State the preparation type.
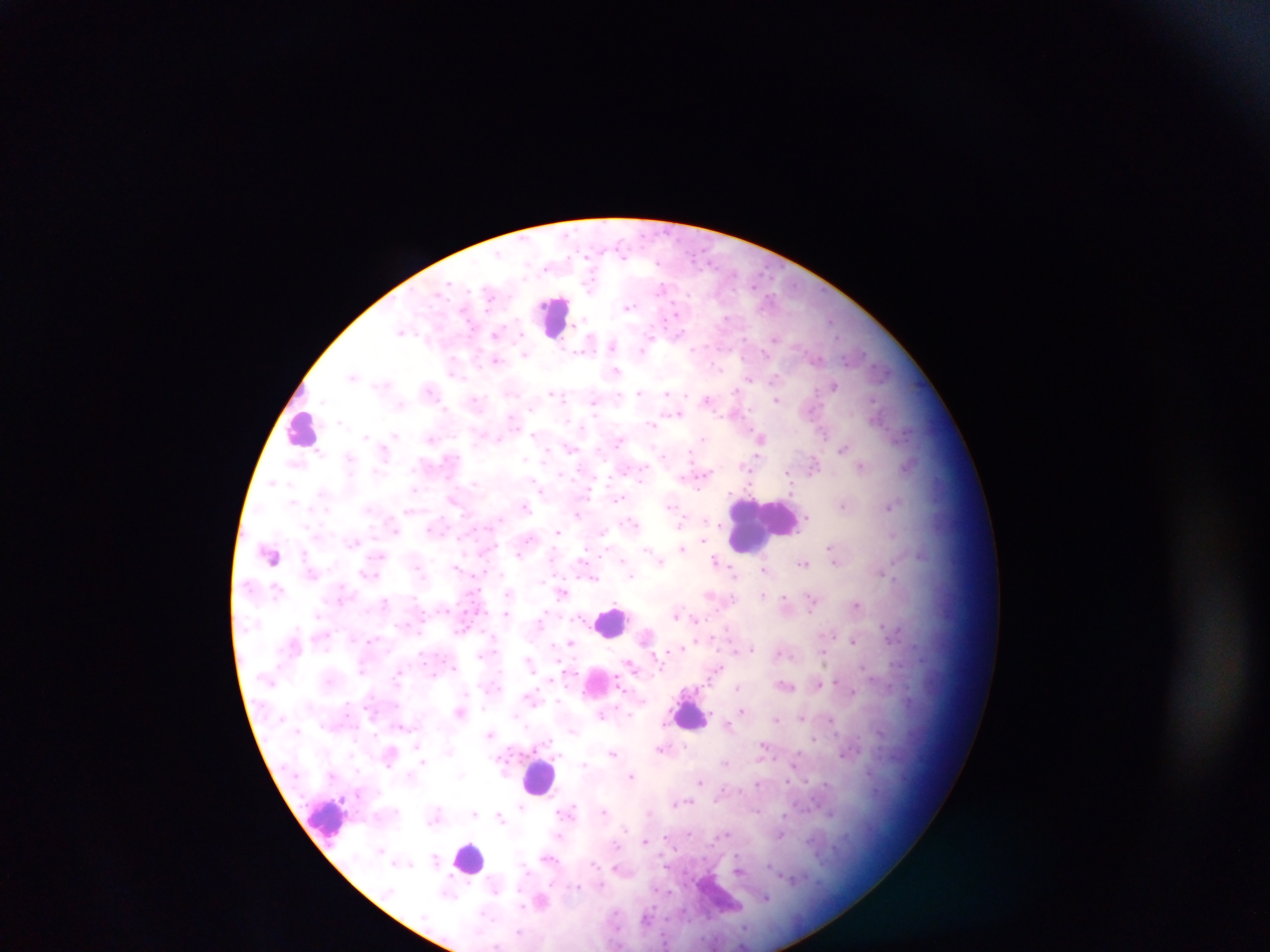
Thick blood film.

Approximate centers as (x, y) in pixels.
Summary:
  - Malaria parasite locations: (628, 307), (401, 331), (497, 333), (774, 338), (612, 345), (614, 352), (526, 353), (496, 360), (616, 371), (354, 375), (775, 376), (749, 378), (834, 384), (639, 391), (668, 392), (554, 393), (708, 398), (776, 399), (475, 400), (594, 400), (677, 413), (432, 438), (703, 438), (761, 438), (844, 447), (385, 450), (663, 455), (814, 463), (862, 465), (789, 474), (272, 481), (415, 488), (541, 490), (619, 498), (454, 500), (844, 505), (524, 506), (889, 506), (577, 513), (683, 519), (680, 524), (717, 526), (558, 531), (893, 534), (702, 541), (682, 549), (833, 552), (659, 559), (716, 561), (805, 562), (457, 568), (765, 569), (734, 573), (367, 574), (632, 574), (594, 576), (562, 592), (764, 594), (711, 595), (386, 601), (785, 601), (812, 602), (856, 604), (506, 615), (677, 615), (696, 620), (648, 635), (853, 640), (570, 642), (750, 648), (675, 650), (735, 651), (781, 652), (823, 652), (529, 661), (632, 665), (362, 666), (718, 667), (399, 672), (820, 683), (785, 685), (738, 687), (853, 692), (532, 697), (744, 710), (461, 711), (602, 713), (802, 716), (778, 718), (830, 719), (403, 724), (664, 724), (728, 726), (490, 733), (815, 739), (417, 745), (764, 747), (663, 749), (614, 753), (726, 763), (424, 764), (584, 765), (632, 776), (701, 781), (675, 802), (686, 802), (522, 806), (568, 811), (605, 811), (831, 812), (474, 814), (501, 817), (725, 835), (781, 835), (560, 836), (645, 840), (435, 857), (549, 858), (619, 869), (740, 870), (497, 888), (448, 894), (766, 898), (541, 900), (647, 920)
  - Leukocyte locations: (553, 316), (303, 429), (763, 523), (611, 622), (689, 714), (539, 776), (328, 818), (469, 859), (715, 895)
  - Field of view: single
  - Capture: mobile-phone photograph through a microscope
  - Country: Ghana
  - Image size: 1270×952 pixels